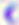
modality = photomicrograph
magnification = 400x
identification = Toxoplasma gondii